Point out each malaria parasite.
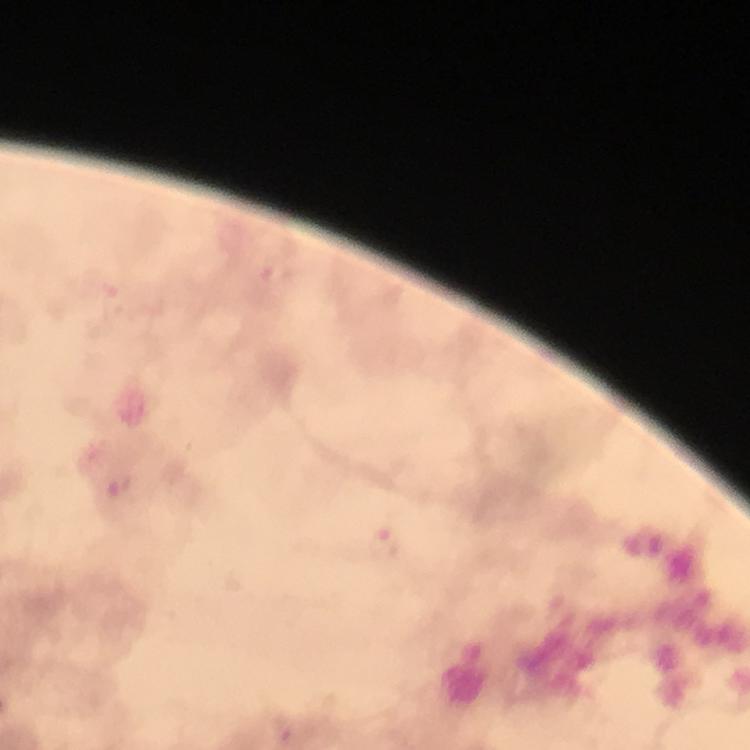
Approximate centers as (x, y) in pixels.
Malaria parasites: (277, 275), (384, 544).

cropped from = a single field of view
immersion oil = applied
magnification = 100x
preparation = thick blood film
stain = Giemsa
context = from a diagnostic examination for malaria
image size = 750×750 pixels
capture = smartphone photograph through a microscope